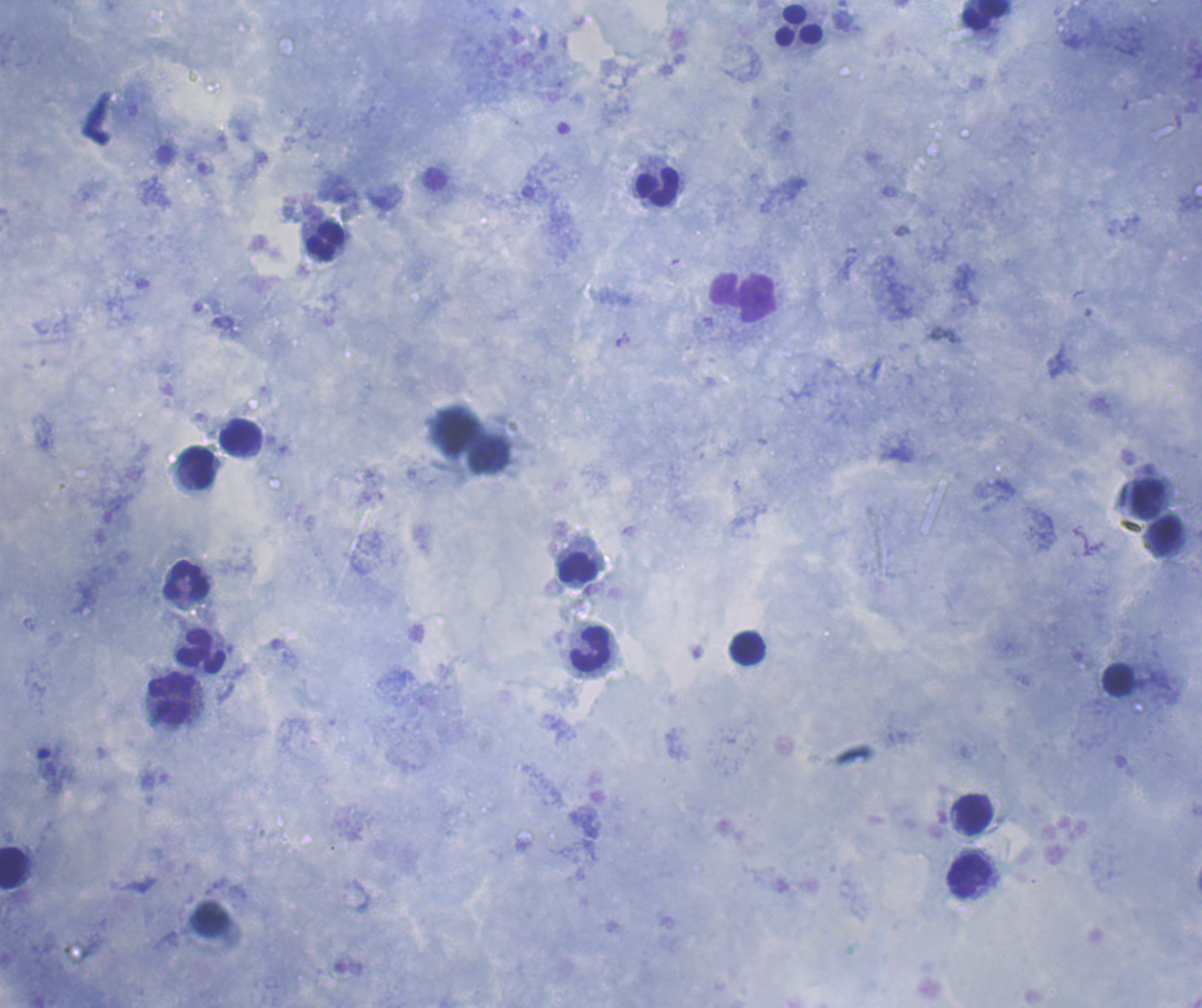

coordinate format = approximate object centers, in pixels from the top-left corner
leukocyte locations = (x=986, y=15), (x=799, y=25), (x=657, y=187), (x=326, y=242), (x=743, y=298), (x=241, y=436), (x=198, y=467), (x=1147, y=498), (x=1165, y=536), (x=578, y=568), (x=186, y=581), (x=748, y=648), (x=591, y=649), (x=201, y=651), (x=1118, y=680), (x=173, y=698), (x=974, y=814), (x=13, y=866), (x=969, y=876)
preparation = thick blood smear
image size = 1202×1008 pixels
background quality = good
context = previously used in an actual diagnosis
result = negative for Plasmodium parasites
coloration quality = good
magnification = 100x
field of view = one from this slide
stain = Romanowsky